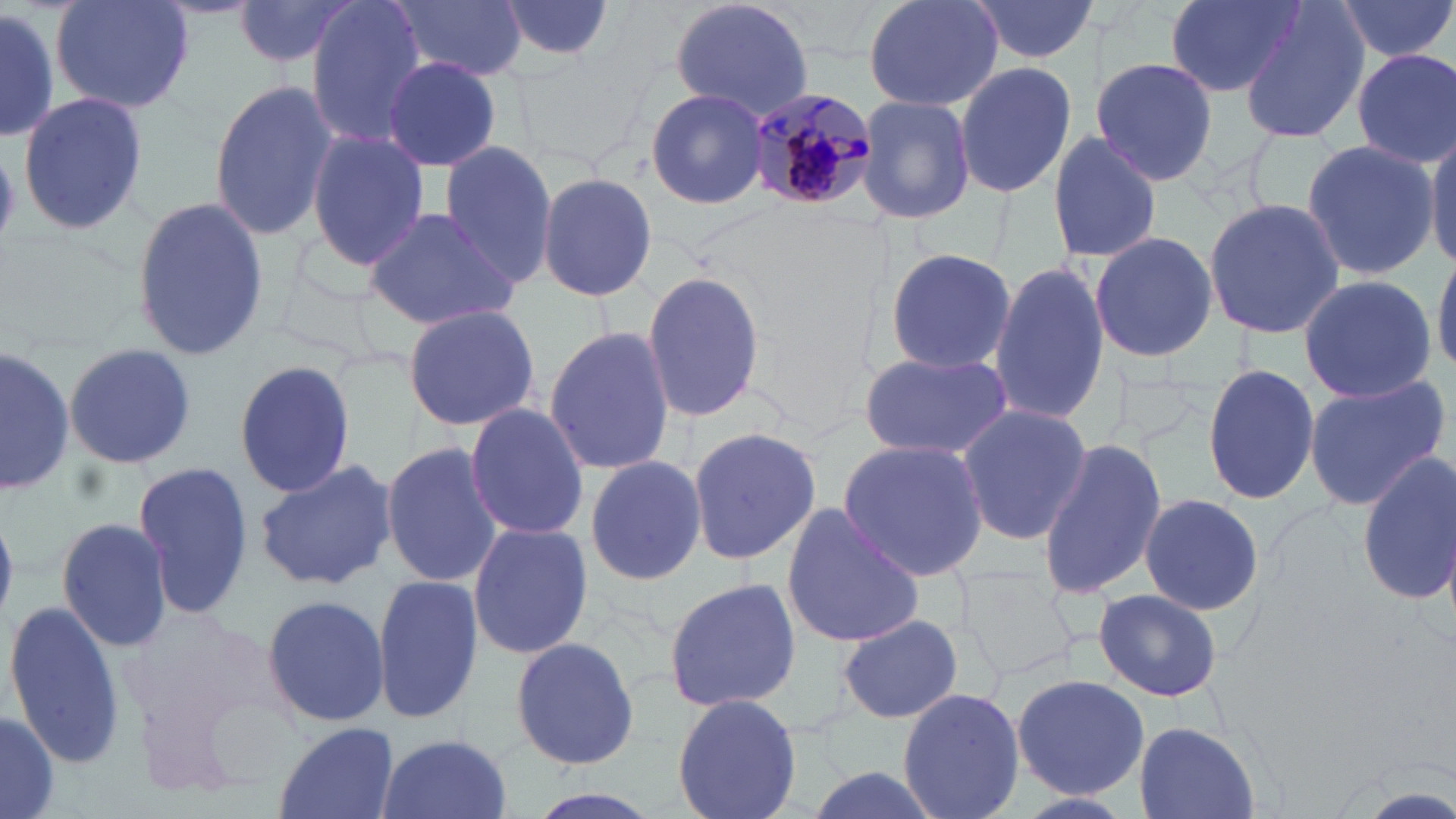 Approximate bounding boxes as named x1/y1/x2/y2 corners in pixels. Uninfected red blood cell locations: (x1=47, y1=0, x2=196, y2=114), (x1=235, y1=0, x2=361, y2=68), (x1=307, y1=0, x2=429, y2=146), (x1=494, y1=0, x2=619, y2=63), (x1=666, y1=0, x2=815, y2=120), (x1=861, y1=0, x2=1007, y2=112), (x1=968, y1=0, x2=1099, y2=63), (x1=1166, y1=0, x2=1302, y2=98), (x1=1334, y1=0, x2=1456, y2=62), (x1=393, y1=1, x2=525, y2=81), (x1=1239, y1=3, x2=1369, y2=144), (x1=0, y1=5, x2=60, y2=144), (x1=1351, y1=49, x2=1456, y2=170), (x1=382, y1=57, x2=502, y2=172), (x1=1092, y1=57, x2=1217, y2=186), (x1=954, y1=60, x2=1077, y2=201), (x1=207, y1=78, x2=338, y2=242), (x1=644, y1=88, x2=769, y2=210), (x1=17, y1=91, x2=147, y2=238), (x1=858, y1=94, x2=976, y2=224), (x1=1426, y1=128, x2=1456, y2=268), (x1=1046, y1=129, x2=1164, y2=264), (x1=305, y1=131, x2=430, y2=272), (x1=1301, y1=138, x2=1438, y2=283), (x1=438, y1=141, x2=557, y2=291), (x1=1, y1=147, x2=28, y2=249), (x1=535, y1=172, x2=659, y2=303), (x1=129, y1=196, x2=268, y2=362), (x1=1204, y1=197, x2=1347, y2=341), (x1=361, y1=205, x2=520, y2=330), (x1=1089, y1=232, x2=1218, y2=362), (x1=882, y1=246, x2=1021, y2=372), (x1=1433, y1=248, x2=1456, y2=378), (x1=988, y1=259, x2=1109, y2=433), (x1=639, y1=269, x2=766, y2=422), (x1=1298, y1=274, x2=1436, y2=402), (x1=401, y1=304, x2=539, y2=431), (x1=543, y1=326, x2=674, y2=474), (x1=63, y1=343, x2=196, y2=469), (x1=1, y1=346, x2=72, y2=500), (x1=859, y1=352, x2=1012, y2=462), (x1=233, y1=356, x2=358, y2=497), (x1=1204, y1=361, x2=1320, y2=508), (x1=1303, y1=374, x2=1451, y2=510), (x1=465, y1=403, x2=590, y2=540), (x1=954, y1=406, x2=1093, y2=545), (x1=688, y1=423, x2=823, y2=568), (x1=1036, y1=436, x2=1166, y2=602), (x1=837, y1=439, x2=992, y2=580), (x1=379, y1=441, x2=504, y2=587), (x1=1354, y1=455, x2=1456, y2=604), (x1=584, y1=457, x2=707, y2=586), (x1=252, y1=459, x2=397, y2=593), (x1=132, y1=462, x2=254, y2=619), (x1=1135, y1=493, x2=1265, y2=614), (x1=779, y1=502, x2=926, y2=650), (x1=56, y1=515, x2=174, y2=651), (x1=467, y1=521, x2=592, y2=659), (x1=371, y1=574, x2=483, y2=725), (x1=662, y1=576, x2=802, y2=715), (x1=1094, y1=588, x2=1223, y2=702), (x1=259, y1=594, x2=389, y2=726), (x1=5, y1=599, x2=124, y2=770), (x1=837, y1=614, x2=963, y2=724), (x1=509, y1=635, x2=641, y2=769), (x1=1011, y1=674, x2=1149, y2=798), (x1=896, y1=687, x2=1026, y2=819), (x1=670, y1=692, x2=805, y2=819), (x1=0, y1=707, x2=60, y2=819), (x1=271, y1=721, x2=400, y2=819), (x1=1132, y1=723, x2=1263, y2=819), (x1=373, y1=733, x2=513, y2=819), (x1=796, y1=762, x2=951, y2=819), (x1=513, y1=787, x2=668, y2=819), (x1=1010, y1=790, x2=1138, y2=819). Plasmodium malariae-infected red blood cell locations: (x1=743, y1=88, x2=877, y2=212). Slide-level diagnosis: Plasmodium malariae. Image is 1456×819 pixels. Captured at 1000x magnification. May-Grünwald-Giemsa-stained preparation. Light microscopy. Thin blood smear. Single field of view.